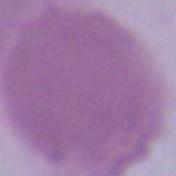

Captured at 1000x magnification. An erythrocyte is seen. Photomicrograph.